Classify this cell by malaria status.
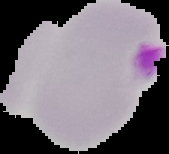

Uninfected.

image type = cell region segmented out of the field of view; surrounding area masked to black
image size = 169×154 pixels
preparation = thin blood film